Locate every blood parasite and identify its species.
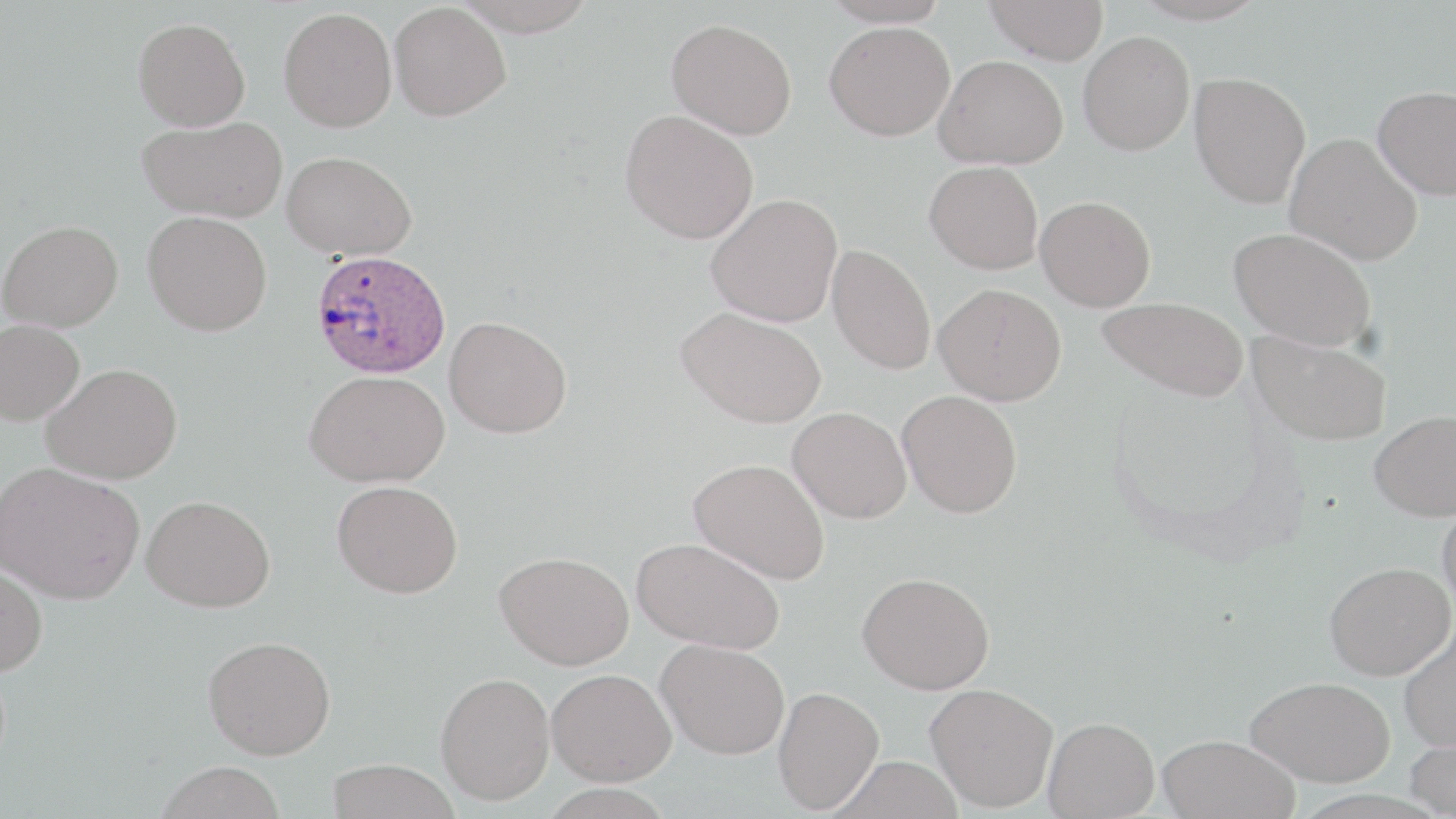
Approximate bounding boxes as named x1/y1/x2/y2 corners in pixels.
Plasmodium ovale-infected red blood cells: (x1=311, y1=249, x2=451, y2=379).
No Plasmodium falciparum, Plasmodium malariae, Plasmodium vivax, Babesia divergens, or Trypanosoma brucei observed.

slide_level_diagnosis: Plasmodium ovale
preparation: thin blood smear
uninfected_red_blood_cell_locations: 'approximate bounding boxes as named x1/y1/x2/y2 corners in pixels: (x1=451, y1=0, x2=598, y2=36), (x1=820, y1=0, x2=954, y2=28), (x1=984, y1=0, x2=1109, y2=64), (x1=389, y1=2, x2=511, y2=121), (x1=278, y1=7, x2=397, y2=132), (x1=133, y1=17, x2=250, y2=131), (x1=666, y1=18, x2=797, y2=140), (x1=824, y1=21, x2=955, y2=141), (x1=1077, y1=31, x2=1195, y2=155), (x1=934, y1=55, x2=1068, y2=169), (x1=1189, y1=72, x2=1311, y2=208), (x1=1373, y1=85, x2=1456, y2=200), (x1=620, y1=109, x2=758, y2=244), (x1=138, y1=116, x2=288, y2=222), (x1=1285, y1=133, x2=1423, y2=266), (x1=282, y1=150, x2=417, y2=260), (x1=924, y1=161, x2=1043, y2=274), (x1=705, y1=194, x2=843, y2=326), (x1=1035, y1=195, x2=1156, y2=311), (x1=142, y1=211, x2=272, y2=334), (x1=1, y1=220, x2=123, y2=331), (x1=1229, y1=227, x2=1377, y2=351), (x1=826, y1=244, x2=936, y2=375), (x1=934, y1=283, x2=1066, y2=405), (x1=1096, y1=296, x2=1249, y2=401), (x1=676, y1=307, x2=826, y2=428), (x1=444, y1=316, x2=571, y2=438), (x1=0, y1=319, x2=85, y2=426), (x1=1246, y1=328, x2=1393, y2=447), (x1=41, y1=362, x2=182, y2=484), (x1=304, y1=370, x2=450, y2=486), (x1=897, y1=389, x2=1022, y2=518), (x1=788, y1=407, x2=911, y2=523), (x1=1369, y1=410, x2=1456, y2=521), (x1=688, y1=458, x2=830, y2=585), (x1=0, y1=461, x2=145, y2=604), (x1=332, y1=480, x2=462, y2=598), (x1=142, y1=495, x2=276, y2=612), (x1=1437, y1=500, x2=1456, y2=613), (x1=632, y1=536, x2=785, y2=654), (x1=495, y1=551, x2=634, y2=669), (x1=0, y1=560, x2=48, y2=677), (x1=1324, y1=561, x2=1455, y2=680), (x1=857, y1=572, x2=995, y2=694), (x1=1399, y1=626, x2=1456, y2=752), (x1=203, y1=636, x2=336, y2=759), (x1=656, y1=638, x2=789, y2=759), (x1=547, y1=668, x2=676, y2=786), (x1=436, y1=672, x2=555, y2=805), (x1=1246, y1=676, x2=1395, y2=786), (x1=925, y1=683, x2=1058, y2=812), (x1=773, y1=687, x2=884, y2=814), (x1=1043, y1=717, x2=1158, y2=818), (x1=1405, y1=730, x2=1456, y2=818), (x1=1157, y1=734, x2=1300, y2=819), (x1=830, y1=756, x2=964, y2=819), (x1=326, y1=759, x2=460, y2=819), (x1=154, y1=761, x2=287, y2=819)'
magnification: 1000x
modality: light microscopy
stain: May-Grünwald-Giemsa
image_size: 1456×819 pixels
field_of_view: single